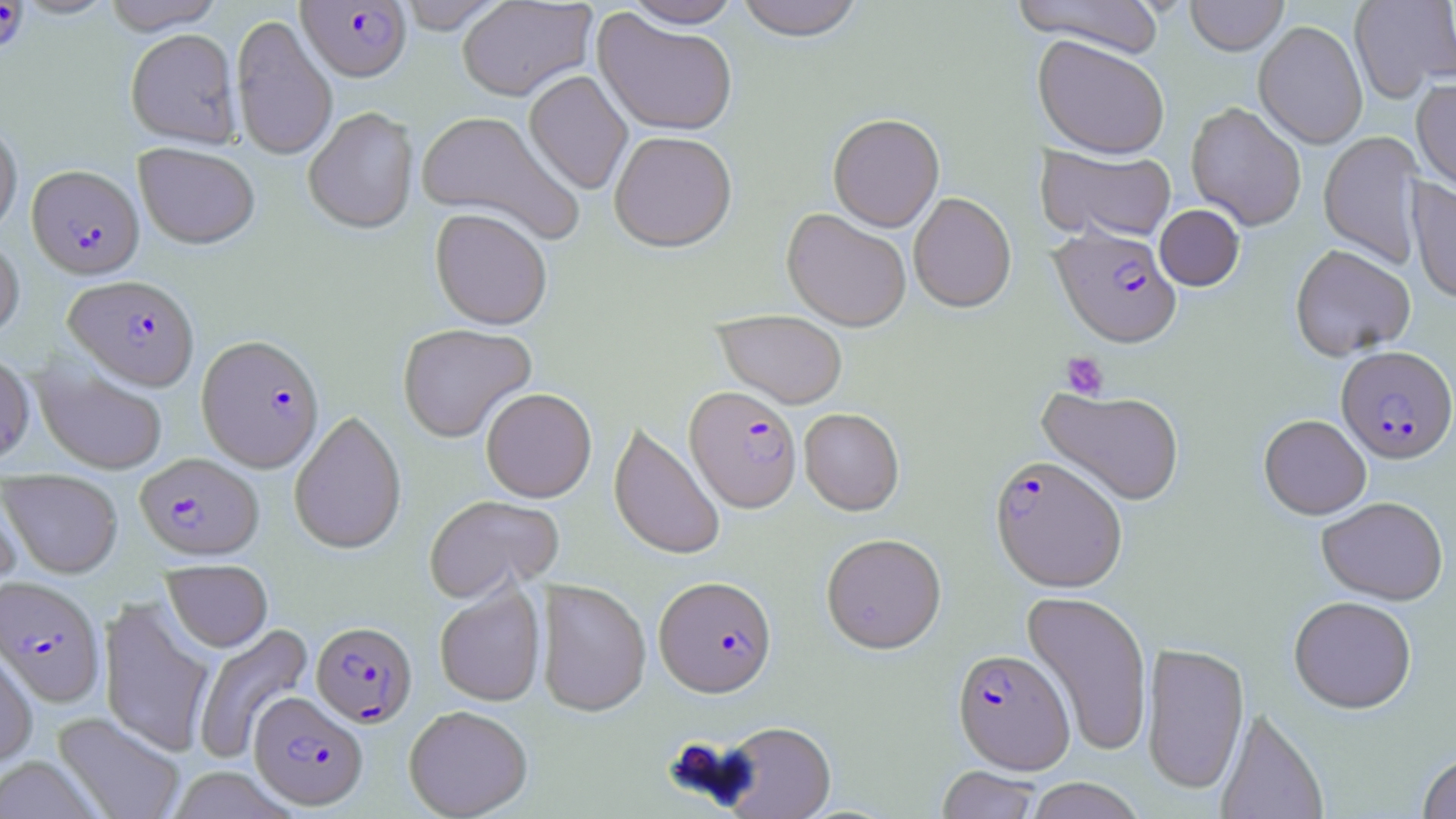
Plasmodium falciparum-infected red blood cell locations = approximate bounding boxes as [x1, y1, x2, y2] in pixels: [1, 0, 30, 56], [297, 1, 413, 84], [26, 166, 144, 280], [1048, 226, 1183, 351], [63, 275, 199, 391], [196, 334, 326, 473], [1336, 346, 1455, 465], [684, 388, 802, 515], [135, 452, 263, 560], [989, 458, 1128, 595], [0, 575, 105, 707], [653, 577, 778, 701], [311, 622, 417, 728], [952, 650, 1075, 776], [249, 693, 368, 811]
slide-level diagnosis = Plasmodium falciparum
platelet locations = approximate bounding boxes as [x1, y1, x2, y2] in pixels: [1060, 351, 1109, 400]
modality = light microscopy
image size = 1456×819 pixels
uninfected red blood cell locations = approximate bounding boxes as [x1, y1, x2, y2] in pixels: [101, 0, 226, 35], [394, 0, 510, 34], [457, 0, 597, 102], [734, 0, 866, 44], [1009, 0, 1166, 58], [1185, 0, 1290, 57], [1349, 0, 1456, 103], [623, 1, 743, 31], [592, 10, 738, 138], [230, 15, 337, 162], [1253, 21, 1368, 150], [126, 29, 242, 148], [1032, 37, 1170, 161], [523, 71, 633, 195], [1411, 78, 1456, 199], [1185, 103, 1306, 232], [303, 108, 418, 236], [414, 111, 581, 243], [827, 116, 944, 234], [0, 118, 22, 237], [1318, 131, 1425, 268], [609, 133, 738, 255], [135, 144, 260, 250], [1036, 146, 1176, 244], [1406, 178, 1456, 306], [908, 194, 1017, 314], [1154, 205, 1245, 292], [430, 210, 552, 332], [781, 210, 911, 333], [0, 234, 24, 342], [1290, 245, 1416, 361], [713, 311, 847, 410], [398, 324, 537, 443], [0, 352, 35, 467], [32, 361, 168, 474], [1036, 387, 1185, 507], [481, 388, 597, 503], [799, 409, 904, 517], [289, 411, 407, 556], [1258, 414, 1371, 521], [608, 423, 725, 562], [2, 470, 123, 579], [0, 478, 23, 598], [424, 494, 565, 604], [1316, 497, 1448, 606], [821, 534, 947, 656], [162, 560, 273, 652], [535, 580, 651, 718], [434, 583, 546, 707], [1020, 591, 1153, 757], [98, 596, 216, 758], [1288, 598, 1417, 715], [193, 622, 315, 764], [0, 643, 38, 770], [1141, 643, 1250, 796], [404, 705, 533, 818], [1215, 708, 1329, 819], [52, 711, 186, 819], [718, 723, 836, 819], [1417, 751, 1456, 818], [0, 756, 105, 819], [165, 766, 297, 819], [936, 768, 1043, 819], [1024, 778, 1147, 819]
field of view = single
preparation = thin blood film
magnification = 1000x
stain = May-Grünwald-Giemsa